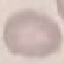

result: negative for malaria parasites
capture: smartphone through the microscope eyepiece
preparation: thin smear
image_type: cell patch, automatically extracted from a larger field of view and resized to 64 × 64 pixels
stain: Giemsa